Classify this cell by malaria status.
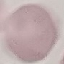
Uninfected.

image_type: automatically extracted cell patch, resized to 64 × 64 pixels
capture: smartphone through the microscope eyepiece
stain: Giemsa
preparation: thin smear